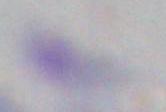 1000x magnification. Photomicrograph. Toxoplasma gondii is seen.